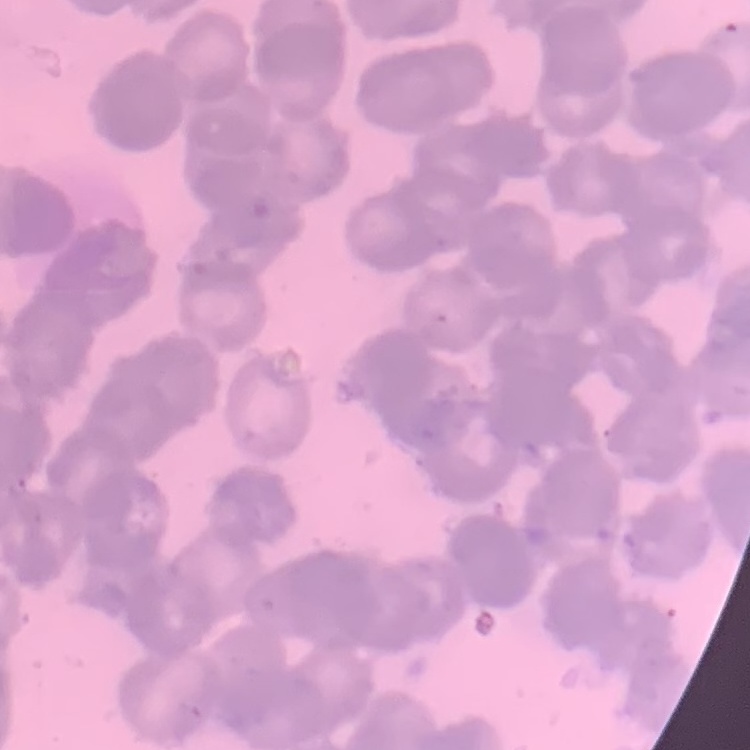

Summary:
  - Erythrocyte morphology: rouleaux formation
  - Preparation: thin blood smear
  - Image type: one tile cut from a larger photomicrograph
  - Stain: Field's or Giemsa